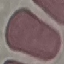
result = no malaria parasites detected
preparation = thin blood smear
image type = automatically extracted cell patch, resized to 64 × 64 pixels
stain = Giemsa
capture = smartphone camera at the microscope eyepiece